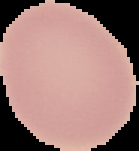
Summary:
  - Image size: 139×151 pixels
  - Preparation: thin blood film
  - Result: negative for malaria parasites
  - Image type: cell region segmented out of the field of view; surrounding area masked to black